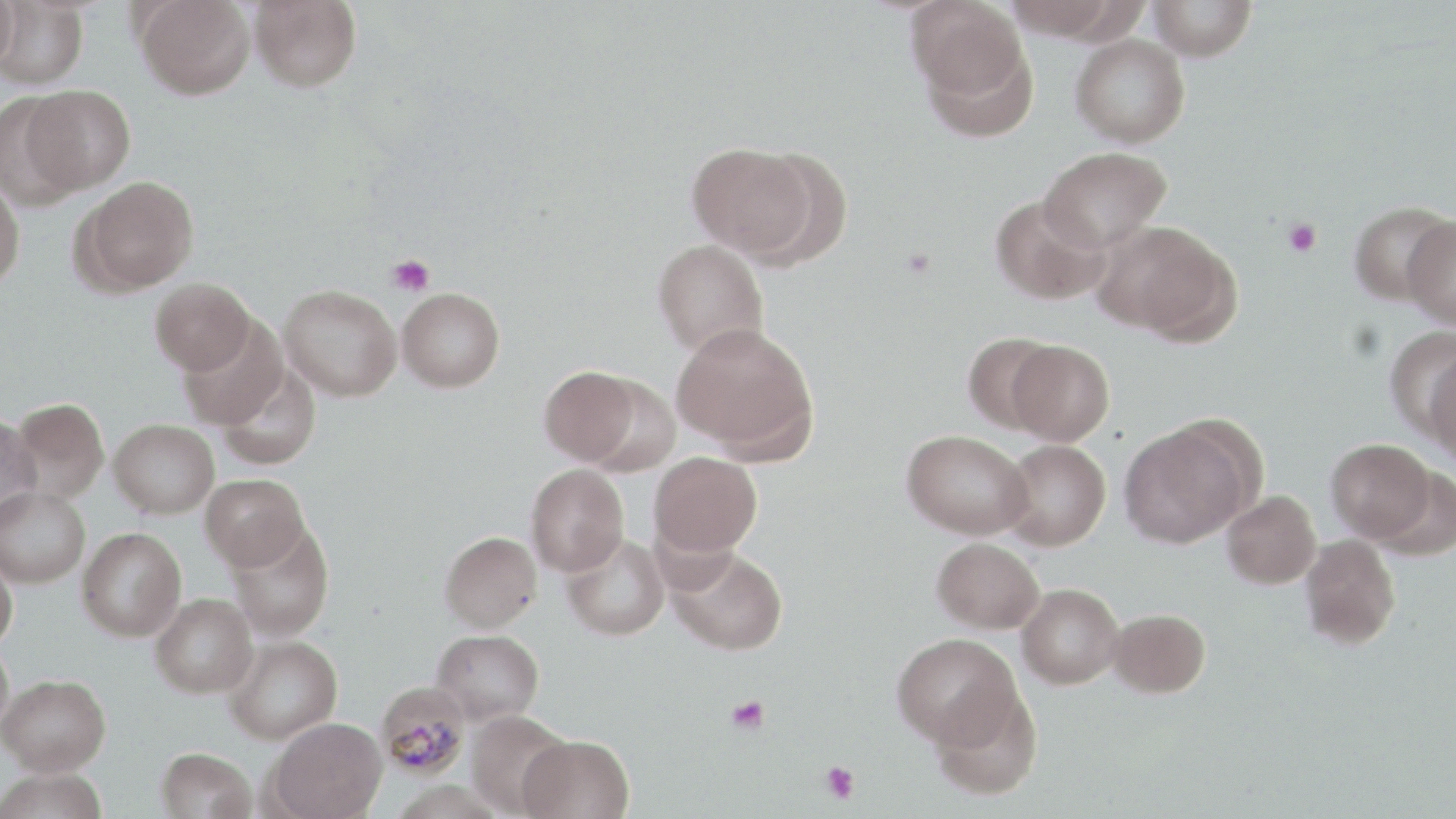
Summary:
  - Coordinate format: approximate bounding boxes as (x1, y1, x2, y2) in pixels
  - Platelet locations: (1283, 218, 1322, 257), (386, 255, 435, 296), (726, 695, 770, 735), (820, 760, 860, 804)
  - Plasmodium malariae-infected red blood cell locations: (376, 682, 471, 780)
  - Uninfected red blood cell locations: (0, 0, 18, 73), (135, 0, 255, 100), (249, 0, 361, 91), (905, 0, 1029, 107), (1001, 0, 1127, 40), (1148, 0, 1257, 61), (0, 1, 88, 89), (1070, 33, 1190, 148), (21, 84, 134, 194), (0, 90, 85, 208), (686, 141, 816, 258), (1040, 146, 1171, 251), (75, 176, 199, 294), (0, 177, 25, 290), (990, 194, 1109, 304), (1349, 201, 1455, 306), (1403, 215, 1456, 329), (1095, 221, 1236, 341), (652, 239, 769, 358), (150, 277, 254, 374), (279, 284, 402, 401), (397, 288, 505, 392), (177, 318, 288, 431), (671, 322, 818, 459), (1387, 328, 1456, 441), (961, 331, 1062, 433), (1006, 339, 1114, 445), (1423, 347, 1456, 465), (216, 363, 321, 470), (539, 366, 641, 466), (10, 397, 109, 502), (0, 416, 42, 525), (108, 418, 219, 518), (1119, 424, 1250, 549), (901, 429, 1032, 538), (1328, 438, 1434, 544), (999, 439, 1111, 550), (649, 451, 762, 556), (525, 463, 629, 575), (1373, 466, 1455, 561), (200, 473, 308, 571), (0, 486, 90, 588), (1221, 491, 1321, 589), (226, 521, 335, 643), (77, 527, 187, 641), (440, 531, 541, 632), (561, 532, 669, 641), (1299, 534, 1401, 650), (932, 537, 1045, 634), (668, 546, 788, 655), (0, 551, 18, 651), (1016, 583, 1123, 688), (150, 593, 258, 698), (1108, 608, 1210, 698), (431, 629, 543, 724), (891, 633, 1020, 748), (224, 634, 342, 743), (0, 637, 14, 737), (1, 674, 110, 775), (930, 685, 1043, 801), (465, 710, 572, 817), (267, 718, 387, 819), (518, 733, 635, 819), (155, 747, 257, 819), (0, 768, 109, 819)
  - Slide-level diagnosis: Plasmodium malariae
  - Modality: optical microscopy
  - Magnification: 1000x
  - Stain: May-Grünwald-Giemsa
  - Preparation: thin blood smear
  - Image size: 1456×819 pixels
  - Field of view: one of a larger specimen